Name the blood parasite species.
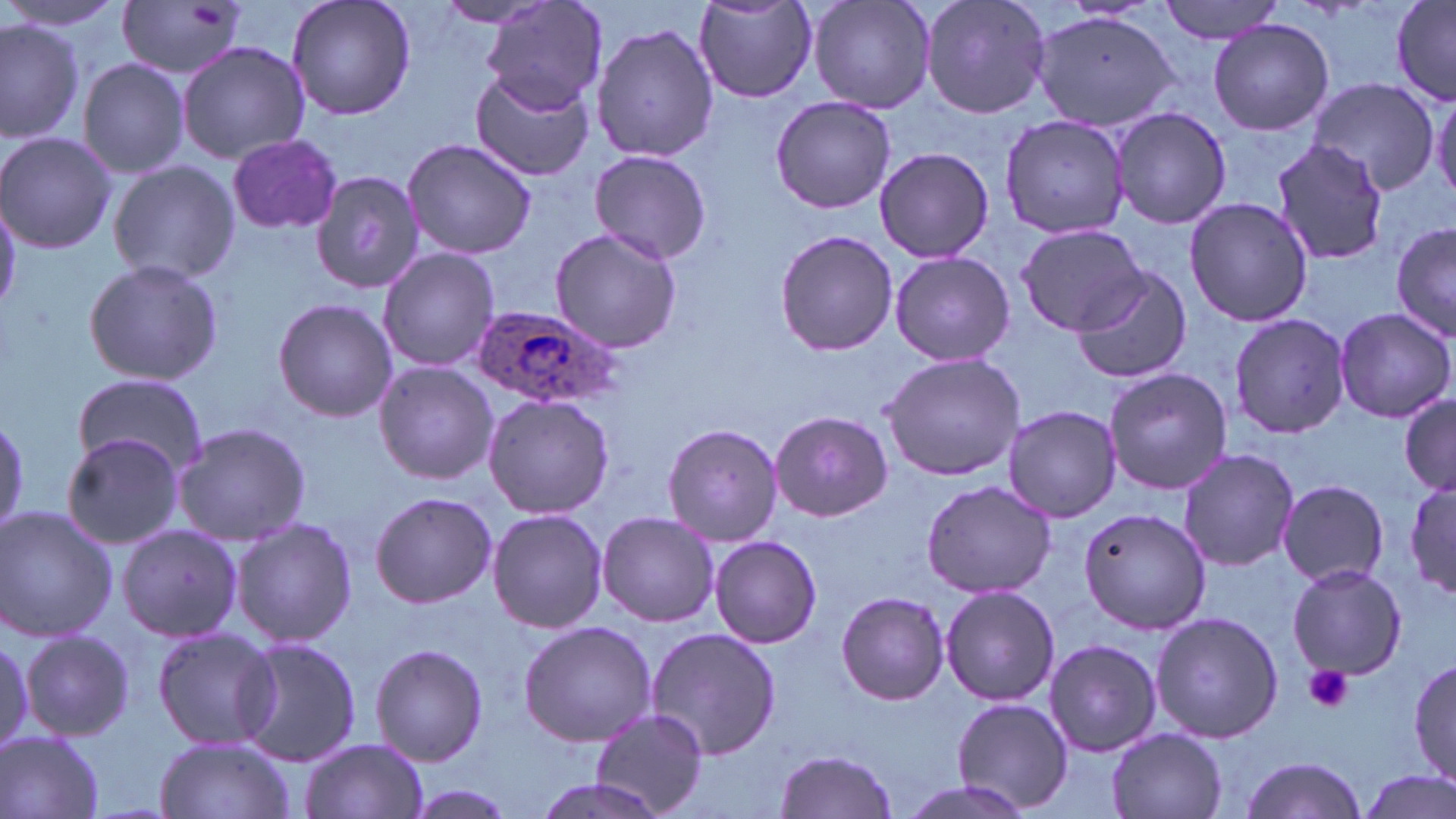

Plasmodium ovale.

Summary:
  - Coordinate format: approximate bounding boxes as named x1/y1/x2/y2 corners in pixels
  - Platelet locations: (x1=190, y1=4, x2=224, y2=30), (x1=1301, y1=664, x2=1354, y2=714)
  - Plasmodium ovale-infected red blood cell locations: (x1=468, y1=303, x2=623, y2=411)
  - Uninfected red blood cell locations: (x1=3, y1=0, x2=121, y2=35), (x1=286, y1=0, x2=416, y2=122), (x1=479, y1=0, x2=607, y2=114), (x1=807, y1=0, x2=936, y2=113), (x1=919, y1=0, x2=1051, y2=121), (x1=1158, y1=0, x2=1290, y2=44), (x1=1390, y1=0, x2=1455, y2=104), (x1=117, y1=1, x2=252, y2=79), (x1=432, y1=1, x2=557, y2=27), (x1=695, y1=2, x2=817, y2=102), (x1=1030, y1=10, x2=1181, y2=132), (x1=0, y1=17, x2=82, y2=143), (x1=1208, y1=18, x2=1335, y2=135), (x1=591, y1=20, x2=718, y2=163), (x1=178, y1=41, x2=309, y2=164), (x1=79, y1=59, x2=189, y2=178), (x1=469, y1=70, x2=594, y2=182), (x1=1308, y1=80, x2=1440, y2=197), (x1=1429, y1=85, x2=1455, y2=205), (x1=770, y1=97, x2=897, y2=213), (x1=1110, y1=106, x2=1233, y2=229), (x1=999, y1=113, x2=1133, y2=241), (x1=0, y1=131, x2=117, y2=254), (x1=227, y1=134, x2=342, y2=233), (x1=400, y1=137, x2=537, y2=260), (x1=1270, y1=141, x2=1392, y2=265), (x1=874, y1=146, x2=994, y2=264), (x1=588, y1=148, x2=712, y2=264), (x1=108, y1=160, x2=240, y2=285), (x1=312, y1=170, x2=424, y2=293), (x1=1, y1=194, x2=21, y2=313), (x1=1183, y1=197, x2=1315, y2=328), (x1=1391, y1=218, x2=1454, y2=345), (x1=1015, y1=222, x2=1147, y2=335), (x1=548, y1=226, x2=683, y2=353), (x1=772, y1=230, x2=901, y2=355), (x1=377, y1=246, x2=500, y2=372), (x1=889, y1=251, x2=1016, y2=367), (x1=83, y1=258, x2=225, y2=387), (x1=1069, y1=266, x2=1193, y2=385), (x1=272, y1=299, x2=398, y2=424), (x1=1333, y1=306, x2=1454, y2=423), (x1=1229, y1=313, x2=1351, y2=439), (x1=881, y1=351, x2=1027, y2=481), (x1=373, y1=360, x2=497, y2=484), (x1=1103, y1=367, x2=1235, y2=496), (x1=72, y1=373, x2=208, y2=477), (x1=482, y1=392, x2=615, y2=519), (x1=1399, y1=392, x2=1456, y2=495), (x1=1001, y1=404, x2=1122, y2=523), (x1=770, y1=410, x2=892, y2=522), (x1=0, y1=414, x2=29, y2=536), (x1=661, y1=422, x2=783, y2=546), (x1=173, y1=424, x2=310, y2=544), (x1=61, y1=433, x2=187, y2=550), (x1=1177, y1=447, x2=1299, y2=572), (x1=1403, y1=474, x2=1453, y2=603), (x1=1277, y1=479, x2=1389, y2=589), (x1=920, y1=480, x2=1061, y2=600), (x1=368, y1=491, x2=498, y2=608), (x1=1075, y1=504, x2=1212, y2=634), (x1=0, y1=506, x2=119, y2=645), (x1=487, y1=507, x2=609, y2=634), (x1=596, y1=509, x2=720, y2=627), (x1=230, y1=518, x2=358, y2=648), (x1=116, y1=523, x2=243, y2=643), (x1=707, y1=535, x2=823, y2=647), (x1=1286, y1=563, x2=1409, y2=680), (x1=941, y1=586, x2=1059, y2=706), (x1=836, y1=591, x2=950, y2=706), (x1=1151, y1=610, x2=1282, y2=743), (x1=518, y1=621, x2=659, y2=747), (x1=152, y1=625, x2=281, y2=751), (x1=644, y1=626, x2=782, y2=761), (x1=21, y1=630, x2=134, y2=742), (x1=0, y1=632, x2=32, y2=754), (x1=235, y1=636, x2=363, y2=767), (x1=1043, y1=638, x2=1162, y2=756), (x1=370, y1=641, x2=489, y2=767), (x1=1410, y1=658, x2=1456, y2=788), (x1=951, y1=696, x2=1072, y2=813), (x1=589, y1=707, x2=709, y2=817), (x1=1107, y1=727, x2=1227, y2=819), (x1=0, y1=729, x2=107, y2=819), (x1=154, y1=735, x2=295, y2=819), (x1=298, y1=737, x2=429, y2=819), (x1=772, y1=749, x2=901, y2=819), (x1=1237, y1=754, x2=1369, y2=819), (x1=1354, y1=768, x2=1455, y2=819), (x1=527, y1=777, x2=673, y2=819), (x1=890, y1=779, x2=1041, y2=819)
  - Preparation: thin blood film
  - Image size: 1456×819 pixels
  - Modality: light microscopy
  - Stain: May-Grünwald-Giemsa
  - Field of view: single
  - Magnification: 1000x